Assess this cell for malaria.
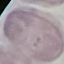

Uninfected.

Summary:
  - Preparation: thin blood film
  - Stain: Giemsa
  - Capture: smartphone through the microscope eyepiece
  - Image type: cell patch, automatically extracted from a larger field of view and resized to 64 × 64 pixels